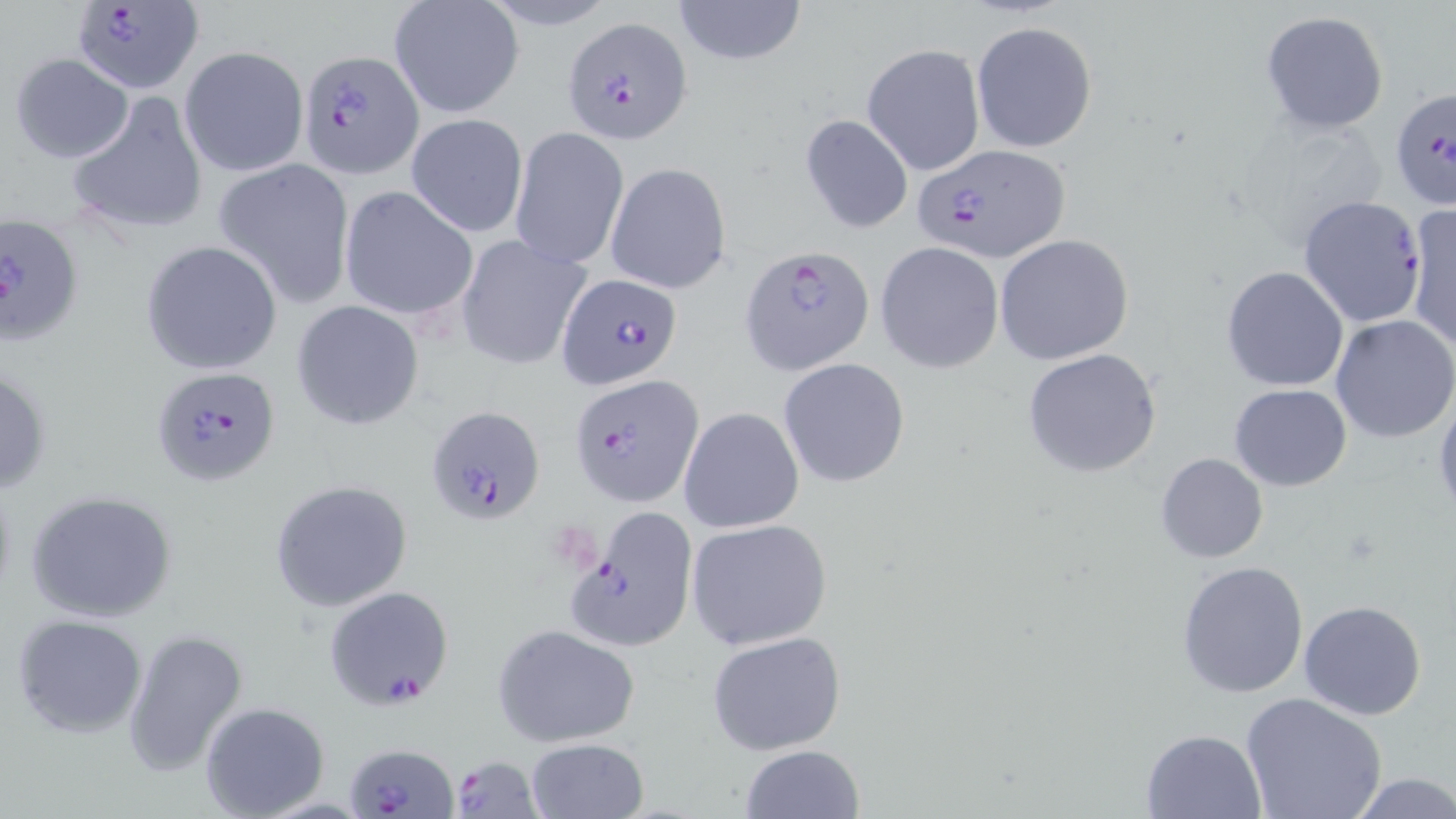
Approximate bounding boxes as (x1, y1, x2, y2) in pixels. Plasmodium falciparum-infected red blood cell locations: (71, 0, 204, 95), (563, 16, 694, 145), (296, 49, 424, 178), (1389, 87, 1456, 216), (911, 142, 1069, 262), (1298, 195, 1427, 328), (0, 214, 85, 345), (740, 245, 875, 375), (556, 273, 684, 391), (150, 365, 280, 486), (570, 373, 705, 507), (426, 404, 545, 525), (567, 503, 701, 653), (322, 584, 453, 709), (346, 740, 459, 818), (447, 755, 544, 818). Uninfected red blood cell locations: (669, 0, 809, 69), (389, 1, 523, 120), (1260, 10, 1389, 134), (971, 20, 1097, 152), (862, 42, 985, 177), (179, 45, 309, 177), (9, 53, 134, 163), (68, 90, 209, 238), (405, 113, 528, 237), (800, 113, 914, 234), (1236, 114, 1389, 244), (510, 126, 629, 269), (213, 159, 354, 304), (605, 161, 732, 294), (340, 186, 478, 321), (1406, 203, 1455, 350), (454, 233, 592, 370), (994, 234, 1134, 365), (139, 240, 282, 375), (874, 241, 1004, 374), (1221, 265, 1349, 392), (290, 299, 425, 431), (1330, 314, 1456, 444), (1022, 348, 1166, 480), (779, 357, 909, 487), (0, 366, 51, 496), (1230, 384, 1350, 491), (1433, 388, 1456, 525), (679, 406, 804, 533), (1156, 451, 1269, 562), (269, 479, 414, 614), (24, 490, 178, 624), (686, 518, 833, 652), (1176, 560, 1310, 699), (1298, 601, 1428, 720), (11, 613, 149, 740), (493, 624, 640, 747), (121, 628, 248, 776), (706, 631, 846, 755), (1239, 692, 1387, 819), (198, 702, 330, 817), (1139, 728, 1269, 816), (523, 737, 651, 819), (737, 744, 868, 819), (1346, 773, 1456, 817). Slide-level diagnosis: Plasmodium falciparum. May-Grünwald-Giemsa-stained preparation. One field of a larger specimen. Thin blood smear. Light microscopy. Captured at 1000x magnification. Image is 1456×819 pixels.